Classify this cell by malaria status.
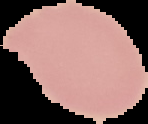

Uninfected.

Summary:
  - Image size: 148×124 pixels
  - Preparation: thin blood film
  - Image type: segmented cell region on a black background